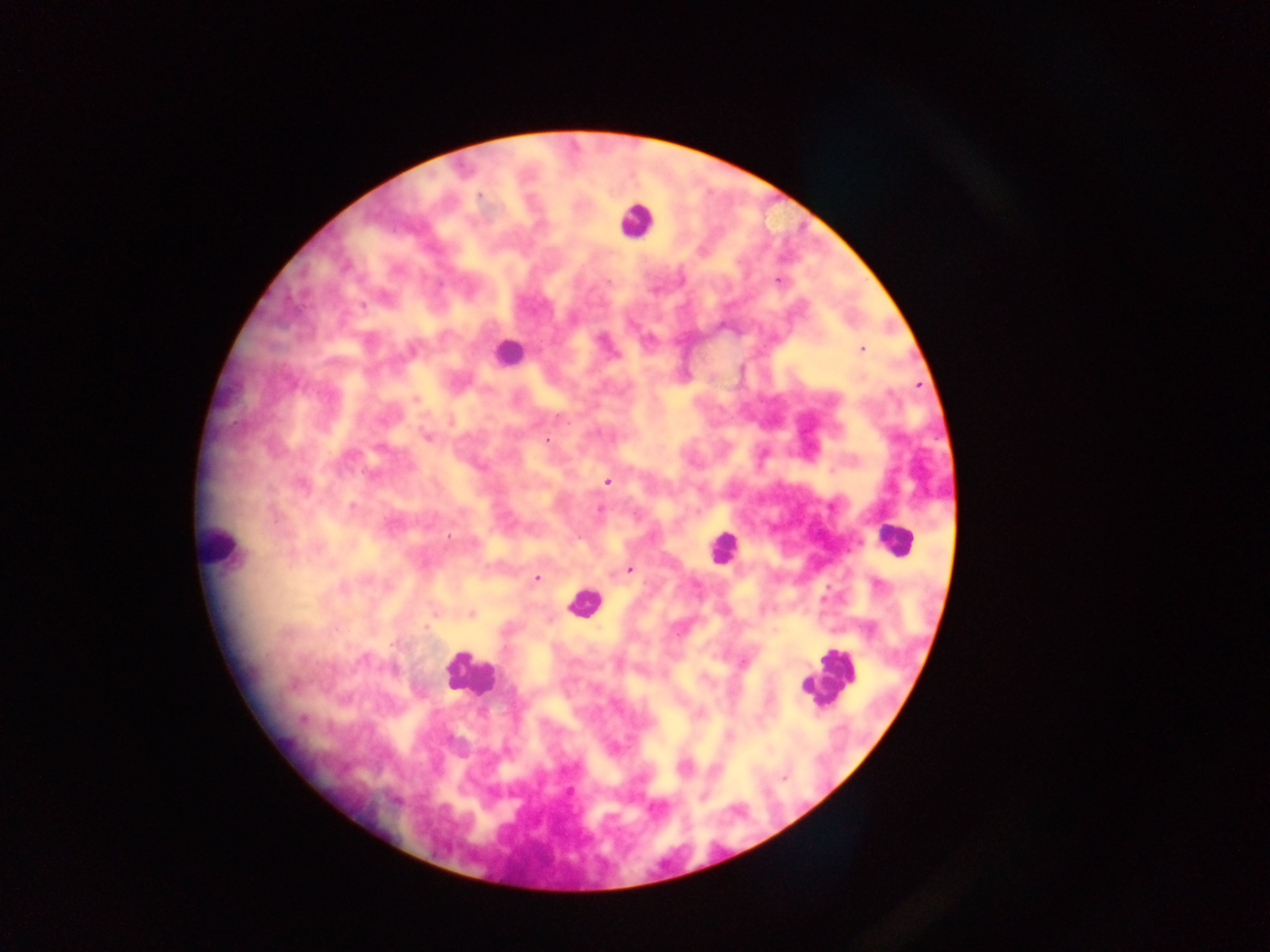
Approximate centers as {x, y} in pixels.
Summary:
  - Leukocyte locations: {636, 220}, {508, 352}, {893, 539}, {221, 546}, {721, 548}, {583, 601}, {469, 674}, {830, 676}, {814, 687}
  - Malaria parasite locations: {480, 195}, {777, 280}, {362, 305}, {861, 349}, {416, 399}, {427, 436}, {547, 441}, {608, 481}, {301, 485}, {352, 507}, {600, 509}, {449, 536}, {629, 569}, {536, 578}, {343, 587}, {472, 614}, {426, 628}, {303, 720}, {730, 736}, {784, 778}, {569, 791}
  - Capture: mobile-phone photograph through a microscope
  - Country: Ghana
  - Field of view: single
  - Preparation: thick blood smear
  - Image size: 1270×952 pixels